Assess this cell for malaria.
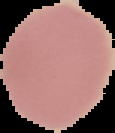
It is uninfected.

From a thin blood smear. Image is 115×133 pixels. Segmented cell region on a black background.